Assess for malaria.
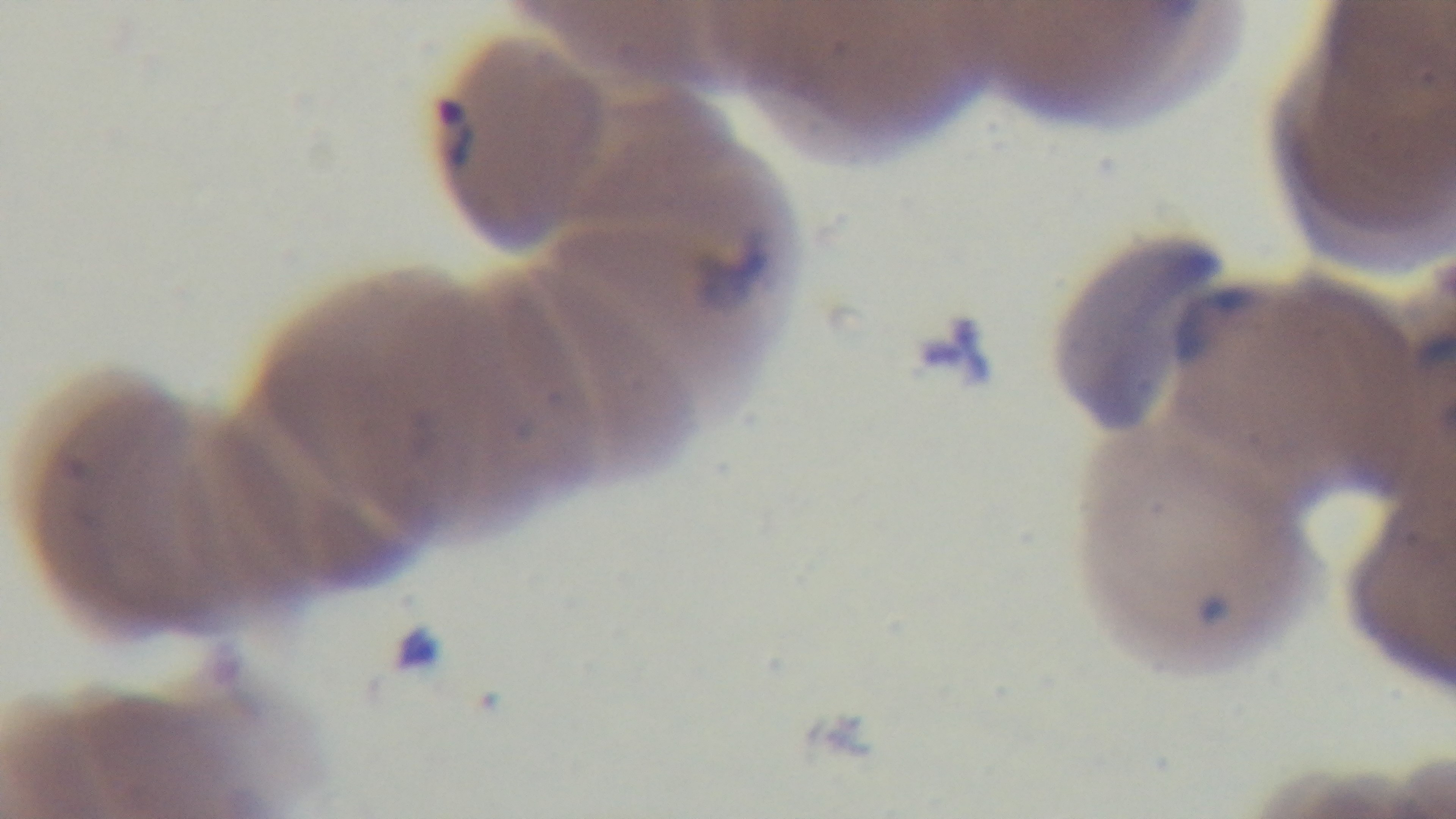
It is infected.

Captured with a mounted 4K digital camera. One field from the slide. Preparation: thin smear. Oil-immersion objective, 100x. Giemsa stain. Photomicrograph.